Report the malaria status of this cell.
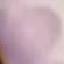

It is uninfected.

Automatically extracted cell patch, resized to 64 × 64 pixels. Acquired by smartphone through the microscope eyepiece. Thin blood film. Giemsa stain.